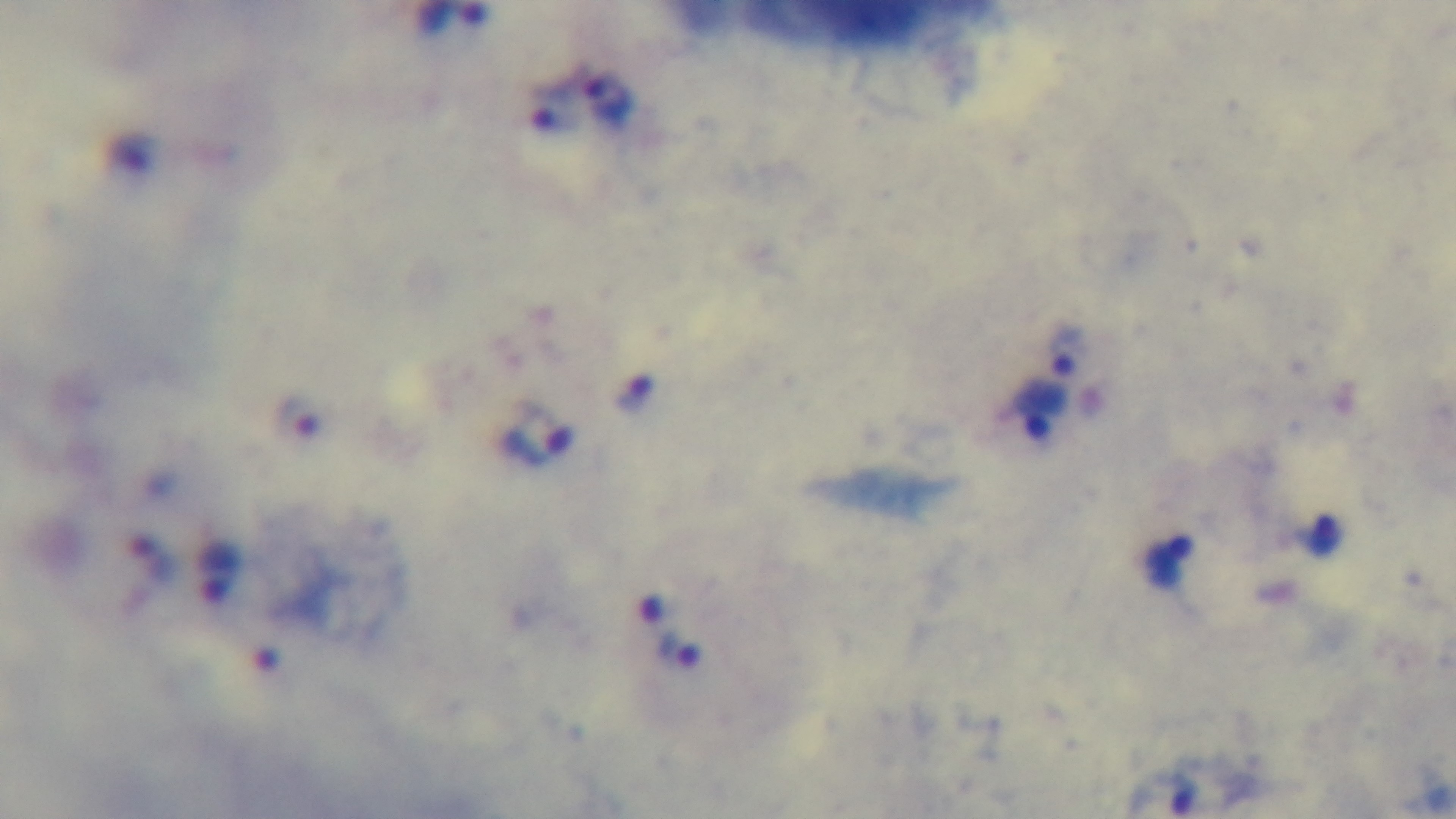 Oil-immersion objective, 100x. Captured with a mounted 4K digital camera. Malaria status: positive. Single field of view. Preparation: thick blood film. Giemsa-stained. Photomicrograph.